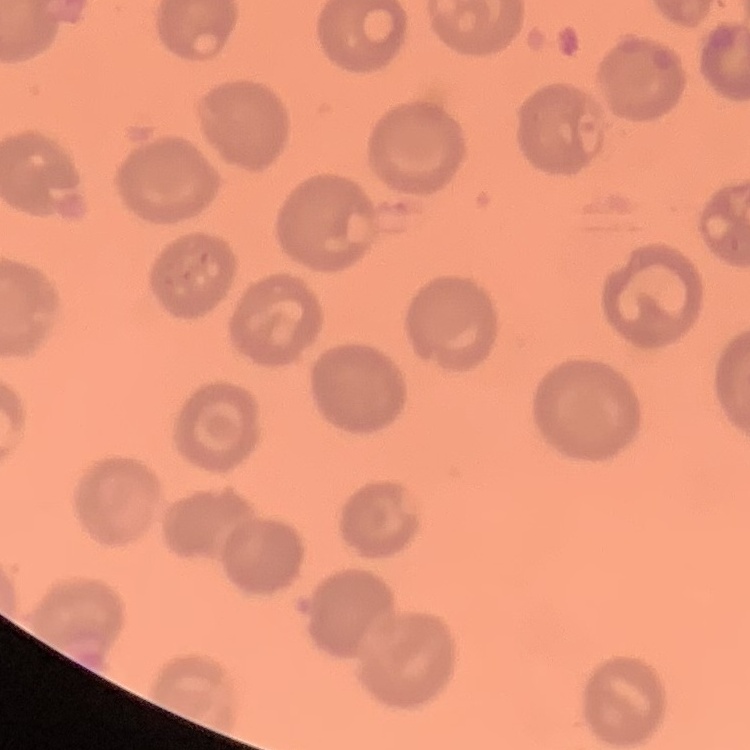

The erythrocytes exhibit no rouleaux formation. Thin peripheral smear. Field's or Giemsa stain. Square crop of a larger photomicrograph.